State the blood parasite species.
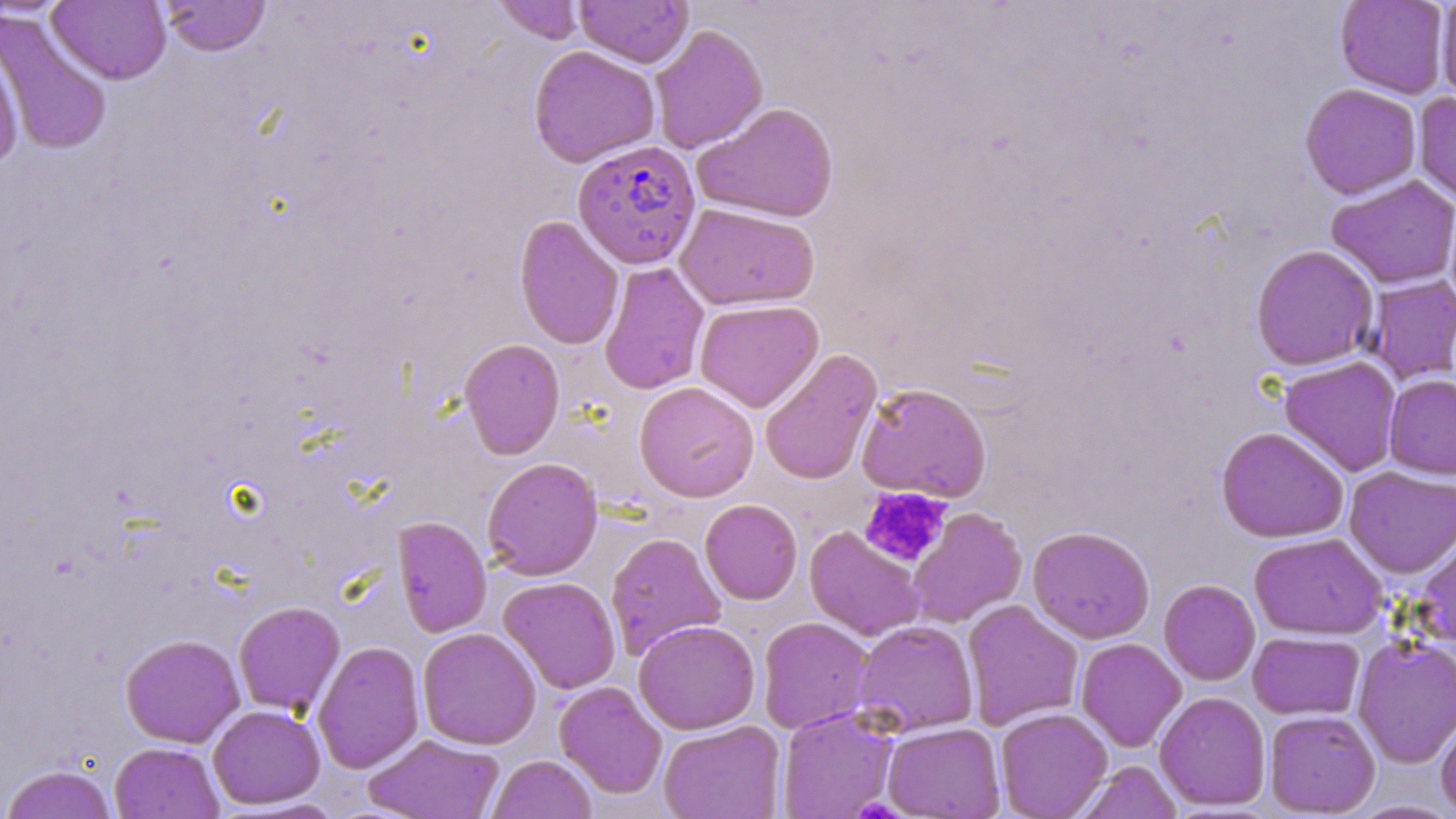
Plasmodium falciparum.

Approximate bounding boxes as [x1, y1, x2, y2] in pixels. Platelet locations: [859, 487, 952, 568], [855, 794, 901, 819]. Plasmodium falciparum-infected red blood cell locations: [572, 139, 702, 270]. Uninfected red blood cell locations: [47, 0, 171, 85], [492, 0, 584, 44], [575, 0, 693, 67], [160, 1, 272, 57], [1335, 1, 1450, 99], [1435, 1, 1456, 104], [1, 11, 113, 158], [648, 24, 768, 154], [0, 32, 25, 171], [528, 45, 661, 168], [1300, 83, 1421, 199], [1413, 92, 1456, 208], [692, 102, 839, 223], [1325, 175, 1456, 289], [1443, 194, 1456, 319], [675, 203, 820, 311], [514, 215, 625, 350], [1250, 244, 1379, 371], [599, 262, 710, 395], [1366, 275, 1456, 384], [694, 299, 824, 413], [459, 338, 565, 459], [759, 348, 883, 485], [1279, 356, 1403, 477], [1384, 374, 1456, 479], [634, 381, 759, 503], [855, 382, 992, 503], [1216, 425, 1349, 543], [481, 457, 603, 581], [1344, 466, 1456, 578], [699, 499, 803, 605], [907, 507, 1028, 628], [392, 515, 491, 638], [1027, 525, 1155, 644], [804, 526, 926, 642], [1415, 529, 1456, 649], [605, 532, 726, 661], [1250, 532, 1389, 639], [498, 576, 621, 694], [1159, 579, 1260, 686], [962, 600, 1084, 731], [233, 601, 345, 716], [757, 616, 873, 734], [633, 619, 760, 735], [852, 619, 979, 737], [417, 627, 541, 750], [1248, 631, 1365, 720], [120, 633, 245, 748], [1352, 635, 1456, 769], [1075, 638, 1187, 753], [312, 641, 425, 774], [554, 681, 668, 799], [1154, 691, 1270, 811], [208, 704, 325, 809], [777, 708, 899, 819], [995, 708, 1113, 819], [1264, 709, 1380, 816], [1435, 710, 1456, 817], [657, 720, 785, 819], [882, 722, 1005, 818], [363, 734, 504, 819], [109, 742, 225, 819], [487, 755, 597, 819], [1076, 761, 1182, 819], [1, 764, 118, 819], [1345, 800, 1456, 818]. Image is 1456×819 pixels. Light microscopy. One field of a larger specimen. 1000x magnification. May-Grünwald-Giemsa-stained preparation. Thin blood film.